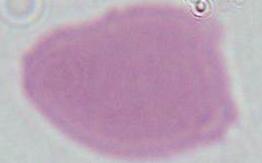

Micrograph. 1000x magnification. An erythrocyte is seen.